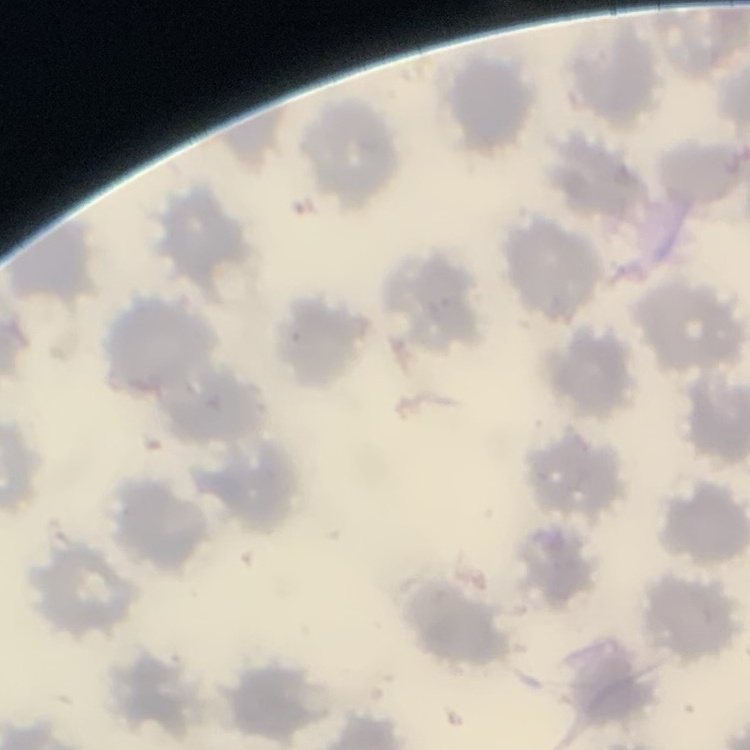
Summary:
  - Erythrocyte morphology: no rouleaux formation
  - Preparation: thin blood film
  - Image type: square crop of a larger photomicrograph
  - Stain: Field's or Giemsa